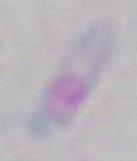
magnification = 1000x
identification = Toxoplasma gondii
modality = micrograph